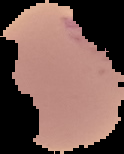
Image is 124×154 pixels. Result: Plasmodium parasites identified. From a thin blood film. The area outside the segmented cell region is set to black.